Locate every Plasmodium parasite.
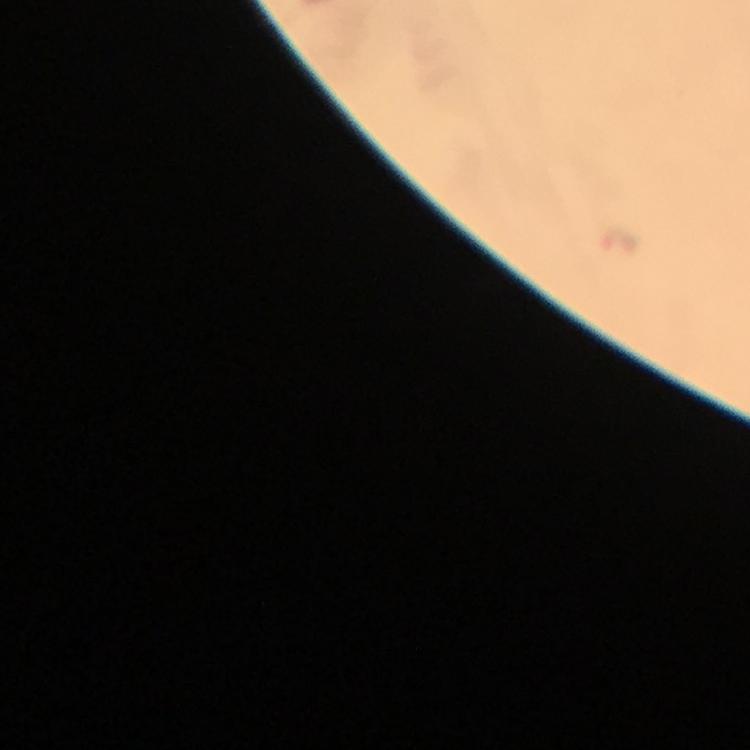

Approximate object centers, in pixels from the top-left corner.
Plasmodium parasites: (x=623, y=244).

Thick blood film. Giemsa-stained preparation. From a malaria diagnostic workup. Image is 750×750 pixels. A crop from one field of view. Photographed through the microscope with a smartphone camera. 100x magnification. Immersion oil was used.